Outline each blood parasite and name the species.
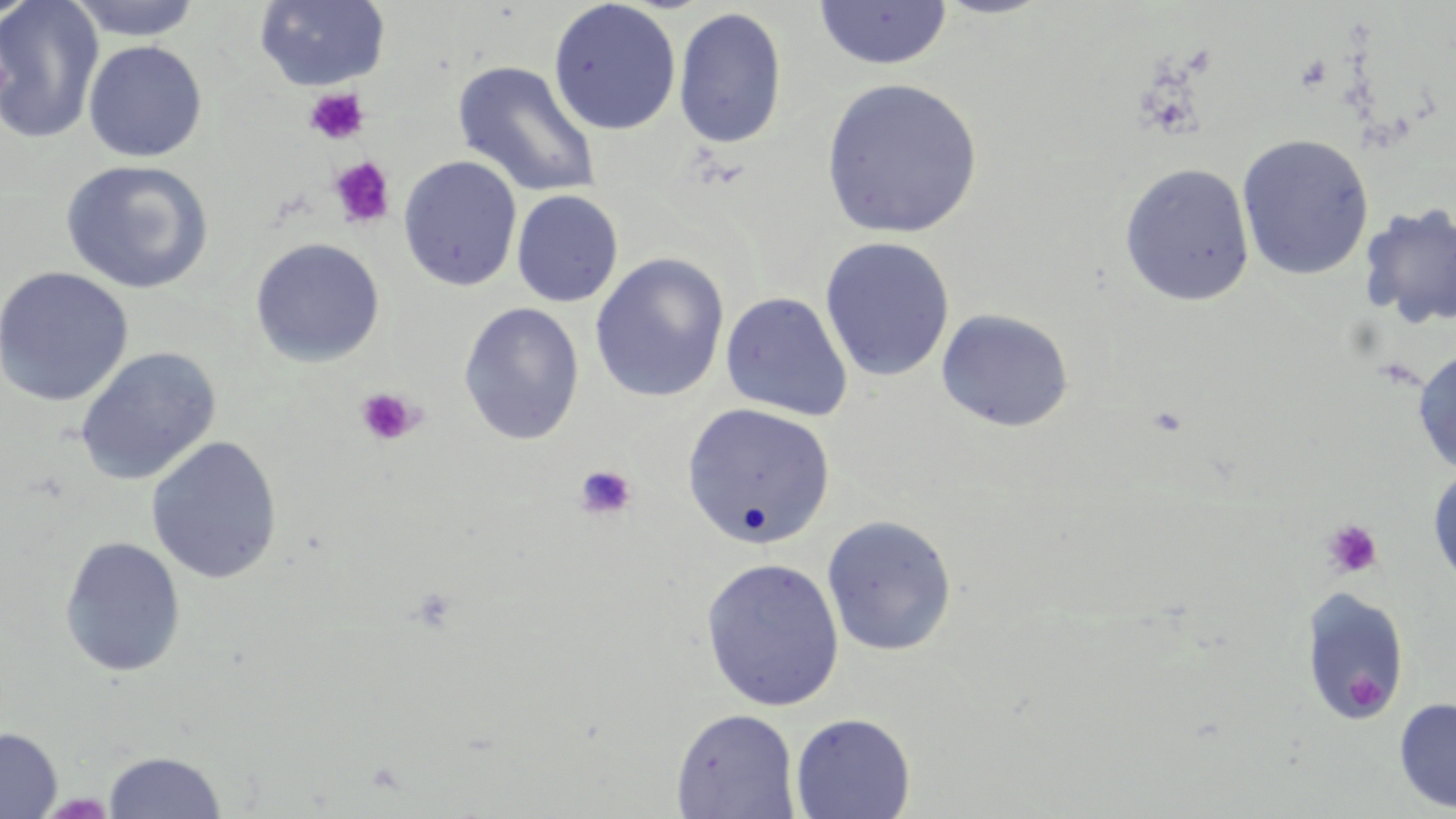
No blood parasites observed.

slide-level diagnosis = no evidence of blood parasites
magnification = 1000x
image size = 1456×819 pixels
modality = optical microscopy
platelet locations = approximate bounding boxes as named x1/y1/x2/y2 corners in pixels: (x1=304, y1=87, x2=369, y2=145), (x1=330, y1=157, x2=396, y2=228), (x1=355, y1=387, x2=421, y2=446), (x1=574, y1=464, x2=636, y2=521), (x1=1322, y1=518, x2=1384, y2=579), (x1=1346, y1=673, x2=1385, y2=714)
field of view = single
preparation = thin blood smear
stain = May-Grünwald-Giemsa
uninfected red blood cell locations = approximate bounding boxes as named x1/y1/x2/y2 corners in pixels: (x1=0, y1=0, x2=104, y2=145), (x1=65, y1=0, x2=204, y2=41), (x1=254, y1=0, x2=391, y2=91), (x1=548, y1=1, x2=681, y2=135), (x1=815, y1=1, x2=953, y2=70), (x1=672, y1=7, x2=788, y2=149), (x1=83, y1=40, x2=207, y2=162), (x1=453, y1=61, x2=601, y2=198), (x1=819, y1=77, x2=983, y2=240), (x1=1236, y1=134, x2=1374, y2=280), (x1=398, y1=156, x2=522, y2=291), (x1=59, y1=160, x2=215, y2=295), (x1=1119, y1=162, x2=1255, y2=306), (x1=511, y1=189, x2=623, y2=307), (x1=1357, y1=202, x2=1456, y2=331), (x1=250, y1=237, x2=385, y2=367), (x1=819, y1=237, x2=955, y2=382), (x1=589, y1=253, x2=729, y2=403), (x1=0, y1=266, x2=134, y2=407), (x1=720, y1=291, x2=852, y2=421), (x1=459, y1=302, x2=584, y2=445), (x1=935, y1=309, x2=1073, y2=432), (x1=74, y1=346, x2=221, y2=486), (x1=1412, y1=347, x2=1456, y2=477), (x1=681, y1=402, x2=836, y2=549), (x1=146, y1=436, x2=283, y2=584), (x1=1427, y1=459, x2=1456, y2=594), (x1=821, y1=514, x2=958, y2=657), (x1=59, y1=536, x2=186, y2=678), (x1=700, y1=557, x2=844, y2=712), (x1=1299, y1=588, x2=1410, y2=726), (x1=1393, y1=696, x2=1456, y2=814), (x1=671, y1=708, x2=801, y2=819), (x1=790, y1=712, x2=915, y2=819), (x1=0, y1=727, x2=62, y2=818), (x1=103, y1=750, x2=226, y2=818)